Identify the blood parasite species.
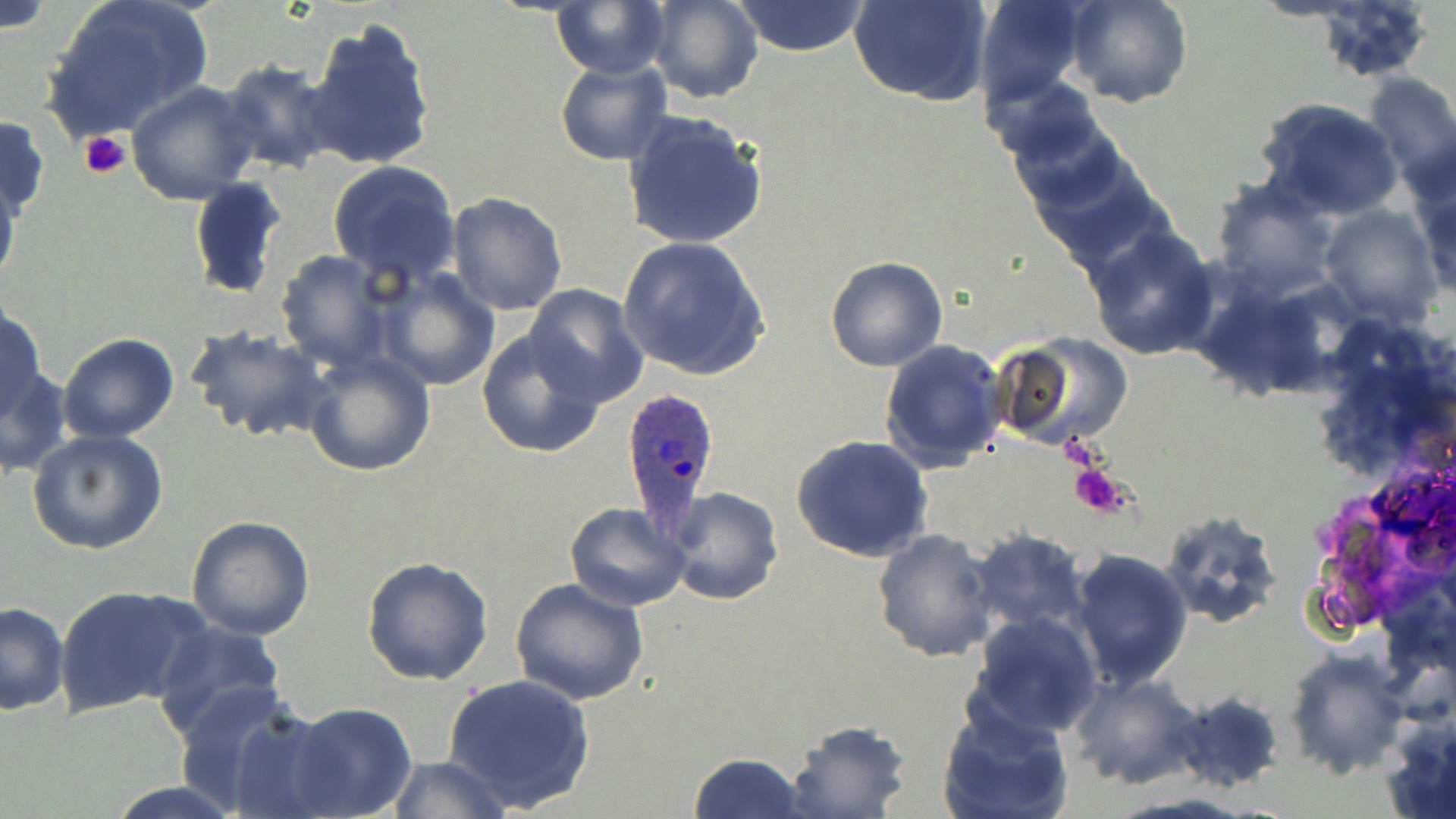
Plasmodium ovale.

Summary:
  - Coordinate format: approximate bounding boxes as (x1,y1)-(x2,y2) corner pairs in pixels
  - Uninfected red blood cell locations: (38,0)-(214,143), (645,0)-(762,104), (851,0)-(992,106), (972,0)-(1088,108), (1063,0)-(1191,108), (0,1)-(55,35), (551,1)-(668,76), (731,1)-(872,57), (302,14)-(438,173), (555,58)-(671,166), (216,60)-(341,176), (1361,72)-(1456,192), (126,82)-(262,205), (1000,87)-(1119,204), (1256,97)-(1403,220), (620,109)-(771,251), (0,112)-(48,224), (1024,144)-(1169,268), (327,160)-(461,286), (1411,163)-(1456,302), (0,172)-(21,295), (1208,175)-(1342,300), (187,177)-(288,300), (445,192)-(568,316), (1317,203)-(1442,328), (1084,225)-(1219,359), (616,234)-(771,382), (274,251)-(391,370), (825,255)-(947,371), (376,265)-(501,391), (524,284)-(649,407), (0,301)-(49,422), (185,327)-(332,444), (475,328)-(607,459), (994,331)-(1132,446), (57,333)-(179,440), (879,338)-(1006,473), (302,350)-(435,477), (1,363)-(73,478), (27,429)-(167,555), (791,434)-(934,563), (660,487)-(783,608), (566,502)-(691,611), (1159,508)-(1281,629), (186,516)-(315,639), (871,528)-(1000,664), (970,528)-(1091,639), (1067,548)-(1193,690), (361,556)-(495,686), (509,577)-(648,705), (54,583)-(210,718), (0,600)-(68,714), (965,612)-(1104,742), (152,619)-(288,742), (1283,648)-(1409,778), (443,672)-(595,812), (1067,672)-(1206,791), (171,686)-(330,817), (1170,689)-(1286,793), (287,703)-(418,817), (938,705)-(1074,819), (1382,713)-(1456,819), (782,719)-(913,818), (688,751)-(808,819), (385,755)-(512,818), (106,781)-(241,818)
  - Plasmodium ovale-infected red blood cell locations: (619,388)-(724,528)
  - Platelet locations: (79,131)-(131,179), (1068,461)-(1133,518)
  - Preparation: thin blood smear
  - Modality: light microscopy
  - Magnification: 1000x
  - Stain: May-Grünwald-Giemsa
  - Field of view: one of a larger specimen
  - Image size: 1456×819 pixels